Name the parasite shown.
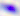

This is Toxoplasma gondii.

modality: photomicrograph
magnification: 400x